Assess the morphology of the red blood cells.
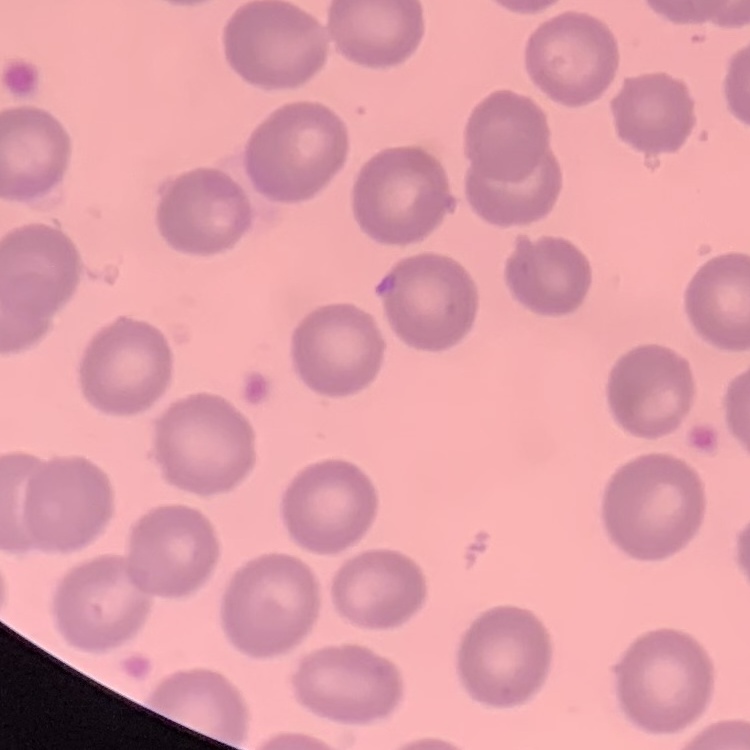

They show no rouleaux formation.

image type = square crop of a larger photomicrograph
preparation = thin peripheral smear
stain = Field's or Giemsa